Locate and identify every blood parasite.
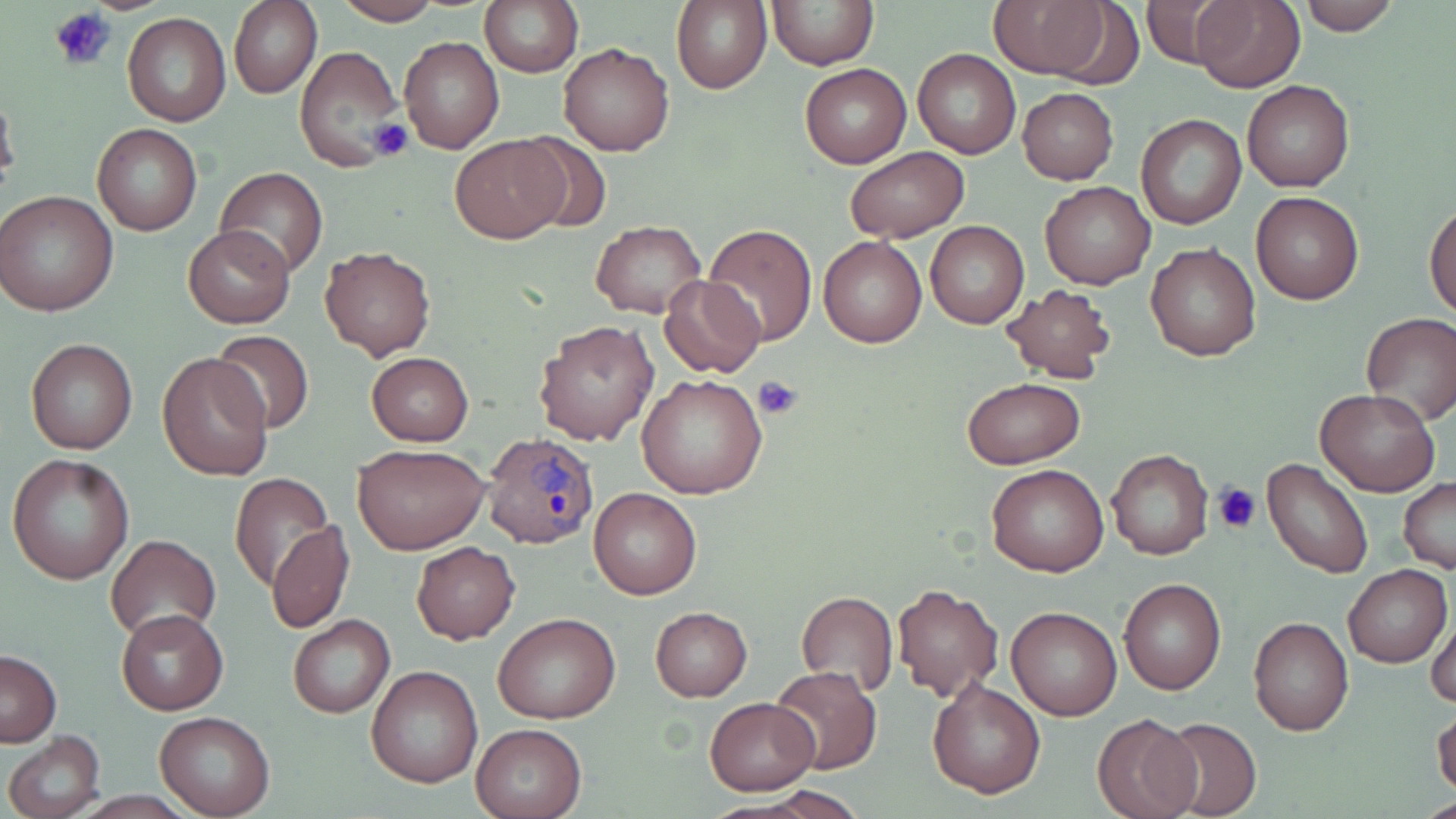
Approximate bounding boxes as (x1, y1, x2, y2) in pixels.
Plasmodium ovale-infected red blood cells: (482, 434, 599, 550).
No Plasmodium falciparum, Plasmodium malariae, Plasmodium vivax, Babesia divergens, or Trypanosoma brucei observed.

slide-level diagnosis = Plasmodium ovale
preparation = thin blood film
uninfected red blood cell locations = approximate bounding boxes as (x1, y1, x2, y2) in pixels: (330, 0, 444, 25), (480, 0, 583, 77), (673, 0, 773, 94), (767, 0, 876, 69), (988, 0, 1111, 80), (1137, 0, 1234, 67), (1190, 1, 1304, 91), (1297, 1, 1400, 35), (228, 2, 321, 99), (122, 12, 232, 126), (399, 36, 503, 155), (557, 41, 674, 155), (296, 46, 406, 176), (913, 48, 1020, 159), (800, 64, 912, 169), (1242, 80, 1354, 193), (0, 85, 19, 200), (1017, 87, 1119, 184), (1136, 114, 1247, 230), (93, 123, 201, 235), (508, 131, 614, 236), (450, 135, 567, 244), (843, 147, 969, 242), (214, 167, 330, 277), (1040, 180, 1155, 290), (1, 191, 118, 317), (1252, 192, 1364, 305), (1209, 198, 1326, 327), (1425, 200, 1456, 318), (926, 220, 1030, 329), (591, 221, 705, 318), (704, 223, 817, 347), (184, 224, 295, 329), (819, 237, 927, 348), (1145, 242, 1260, 360), (318, 246, 435, 361), (659, 274, 766, 378), (999, 284, 1117, 384), (1360, 314, 1456, 426), (533, 319, 658, 445), (208, 329, 316, 435), (25, 339, 137, 453), (157, 351, 273, 480), (366, 352, 473, 446), (637, 374, 766, 500), (961, 376, 1086, 469), (1315, 388, 1439, 495), (352, 442, 489, 554), (1107, 449, 1214, 560), (6, 454, 134, 585), (1262, 457, 1375, 581), (987, 463, 1109, 578), (228, 473, 336, 590), (1399, 477, 1456, 571), (588, 487, 702, 599), (268, 521, 354, 633), (105, 534, 223, 641), (412, 541, 521, 643), (1343, 564, 1451, 667), (1118, 575, 1226, 695), (893, 582, 1003, 701), (794, 590, 897, 698), (650, 606, 752, 702), (1007, 606, 1122, 721), (115, 607, 229, 715), (1427, 607, 1456, 710), (492, 612, 621, 724), (288, 614, 394, 718), (1248, 615, 1354, 737), (0, 649, 61, 746), (366, 665, 484, 789), (767, 666, 882, 774), (928, 678, 1046, 799), (704, 696, 820, 795), (1432, 706, 1456, 800), (154, 712, 274, 817), (1094, 713, 1199, 819), (1157, 717, 1262, 819), (470, 723, 587, 819), (4, 731, 106, 817)
stain = May-Grünwald-Giemsa
image size = 1456×819 pixels
modality = optical microscopy
field of view = single
magnification = 1000x
platelet locations = approximate bounding boxes as (x1, y1, x2, y2) in pixels: (51, 6, 116, 71), (366, 118, 414, 161), (753, 374, 803, 418), (1213, 481, 1261, 534)